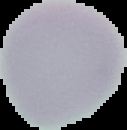
Image is 127×130 pixels. Malaria status: uninfected. Cell region segmented out of the field of view; the surrounding area is masked to black. From a thin blood film.